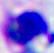
{
  "identification": "leukocyte",
  "magnification": "400x",
  "modality": "photomicrograph"
}